Outline each blood parasite and name the species.
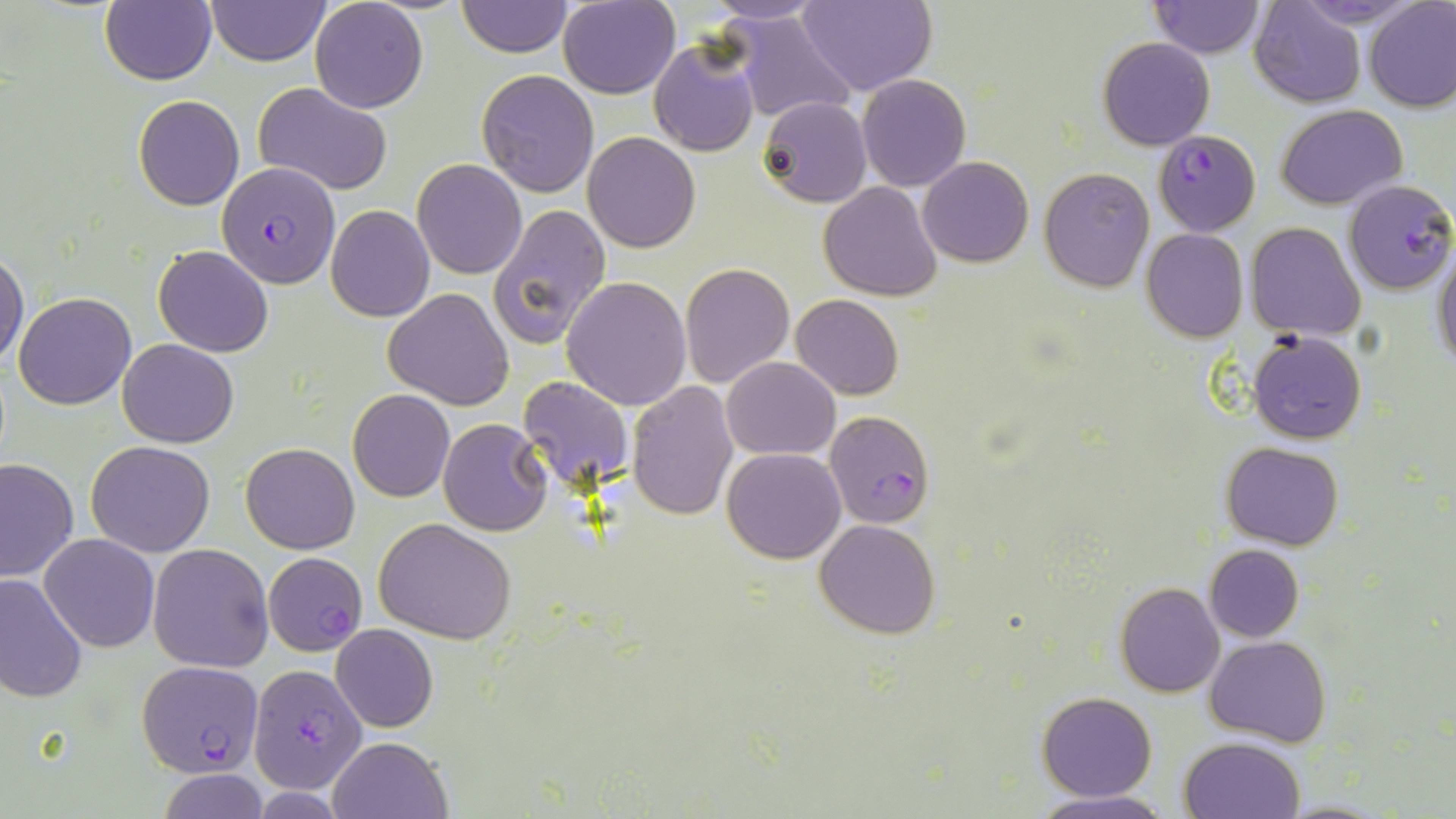

Approximate bounding boxes as (x1,y1)-(x2,y2) corner pairs in pixels.
Plasmodium falciparum-infected red blood cells: (1155,131)-(1261,235), (216,161)-(342,289), (1343,179)-(1456,296), (825,409)-(935,530), (263,553)-(368,657), (135,660)-(264,777), (249,663)-(366,792).
No Plasmodium ovale, Plasmodium malariae, Plasmodium vivax, Babesia divergens, or Trypanosoma brucei observed.

slide-level diagnosis = Plasmodium falciparum
preparation = thin blood smear
field of view = single
magnification = 1000x
image size = 1456×819 pixels
stain = May-Grünwald-Giemsa
modality = optical microscopy
uninfected red blood cell locations = approximate bounding boxes as (x1,y1)-(x2,y2) corner pairs in pixels: (310,0)-(428,113), (456,0)-(572,57), (557,0)-(679,99), (1249,0)-(1366,108), (1362,0)-(1456,112), (205,1)-(329,66), (707,1)-(829,26), (796,1)-(936,97), (1147,1)-(1265,57), (100,2)-(216,86), (727,9)-(856,125), (1098,37)-(1215,150), (647,38)-(761,155), (476,69)-(600,196), (857,73)-(970,192), (252,83)-(394,196), (133,95)-(245,210), (758,96)-(872,207), (1277,104)-(1406,208), (583,131)-(700,253), (919,156)-(1034,267), (412,158)-(526,279), (1039,167)-(1155,292), (344,178)-(520,303), (819,183)-(943,300), (486,202)-(611,349), (325,204)-(434,321), (1245,221)-(1365,339), (1141,229)-(1249,343), (153,246)-(273,357), (1433,248)-(1456,372), (0,252)-(28,371), (680,262)-(794,388), (561,276)-(693,410), (383,288)-(514,410), (13,292)-(136,410), (791,294)-(903,400), (1248,329)-(1366,443), (117,339)-(239,448), (721,358)-(839,459), (518,375)-(634,493), (627,383)-(738,521), (346,389)-(455,503), (437,418)-(553,536), (86,441)-(215,557), (240,442)-(360,554), (1222,442)-(1344,549), (722,447)-(847,564), (0,457)-(78,583), (374,518)-(516,644), (815,518)-(940,639), (40,533)-(159,652), (148,543)-(274,672), (1204,544)-(1304,641), (0,575)-(89,703), (1114,582)-(1224,697), (331,624)-(439,732), (1205,635)-(1330,747), (1036,691)-(1157,801), (328,735)-(451,819), (1179,735)-(1306,819), (156,768)-(269,819), (1028,789)-(1173,818), (1278,799)-(1389,817)